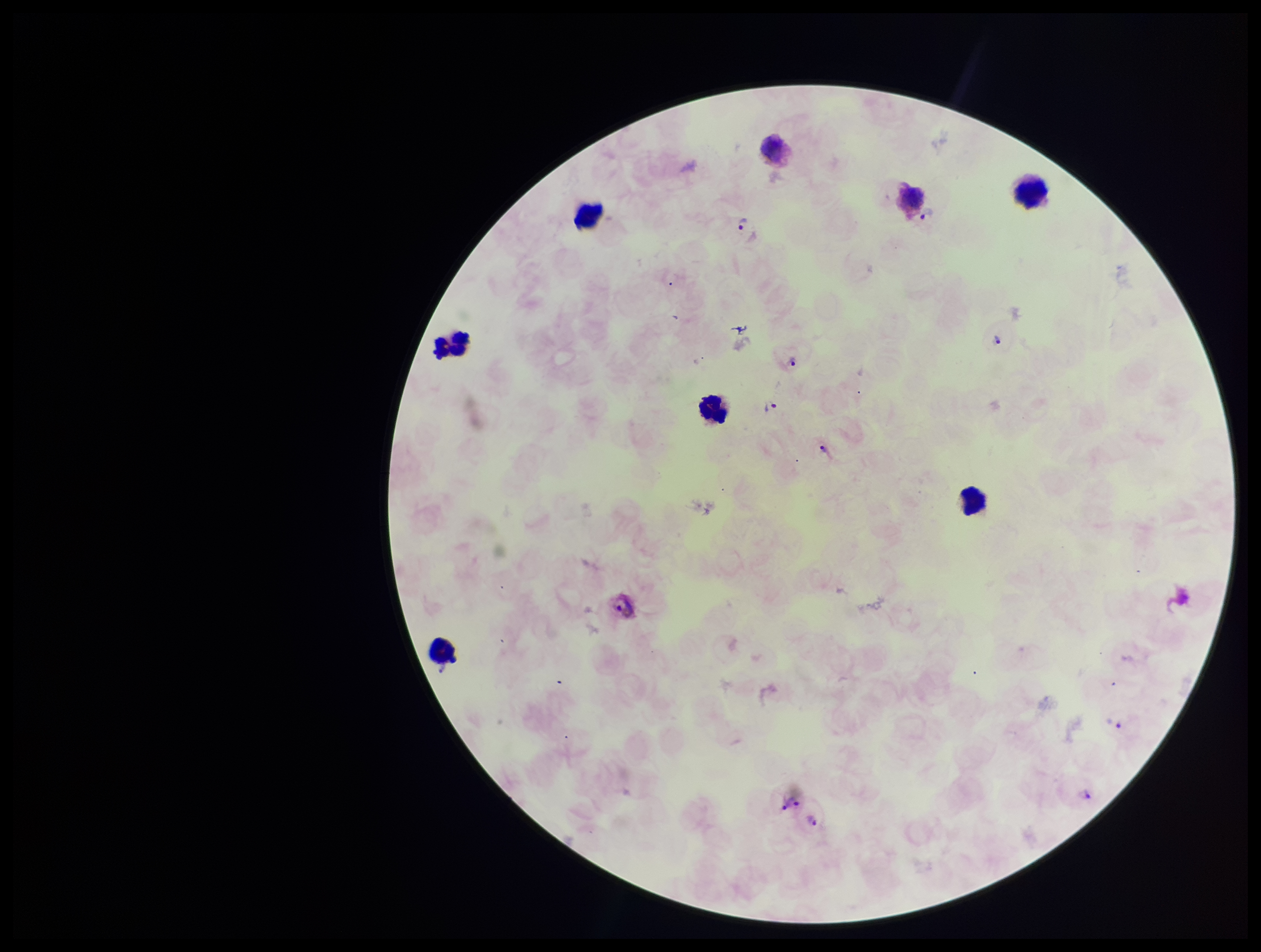
Summary:
  - Preparation: thick blood smear
  - Patient malaria status: positive
  - Plasmodium parasites: identified
  - Leukocyte count: 8
  - Image size: 1261×952 pixels
  - Capture: smartphone photograph through the microscope eyepiece
  - Stain: Giemsa
  - Species reported for this patient: Plasmodium vivax
  - Field of view: single
  - Parasite count: 9